State which parasite is depicted.
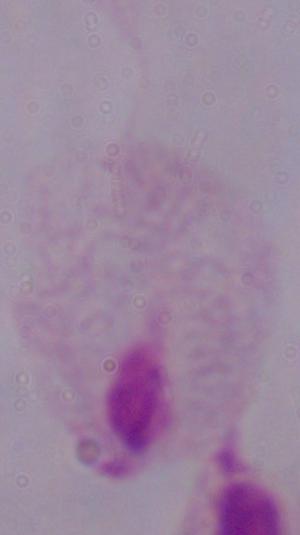

This is a trichomonad.

magnification = 1000x
modality = micrograph